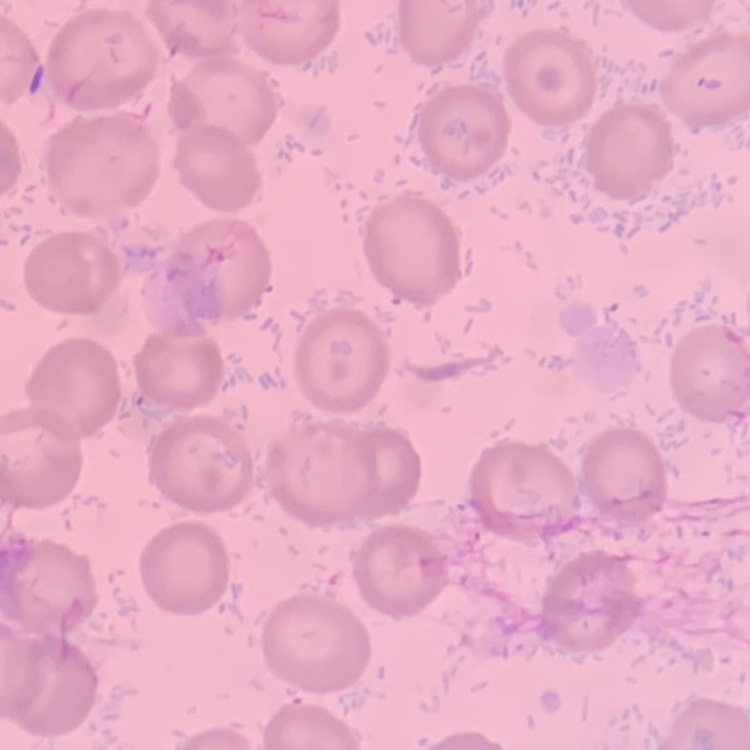

{
  "red_blood_cell_morphology": "no rouleaux formation",
  "preparation": "thin blood smear",
  "image_type": "one tile cut from a larger photomicrograph",
  "stain": "Field's or Giemsa"
}